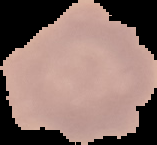

Summary:
  - Result: no Plasmodium parasites detected
  - Image type: segmented cell region on a black background
  - Preparation: thin blood smear
  - Image size: 157×145 pixels